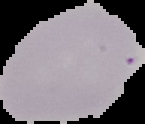 Cell region segmented out of the field of view; the surrounding area is masked to black. Malaria status: uninfected. From a thin blood smear. Image is 145×124 pixels.